Identify the blood parasite species.
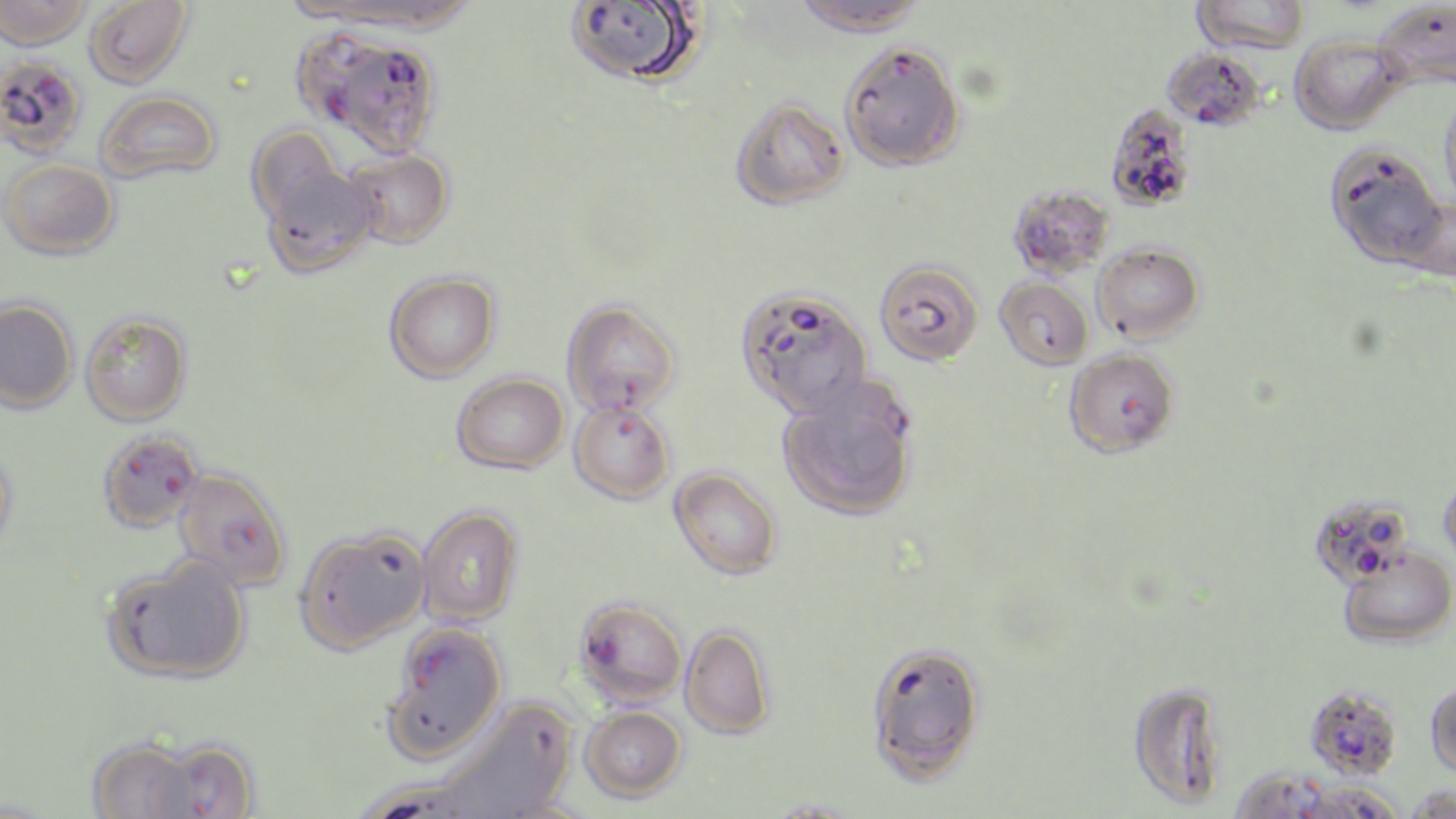

Plasmodium falciparum.

stain = May-Grünwald-Giemsa
magnification = 1000x
uninfected red blood cell locations = approximate bounding boxes as [x1, y1, x2, y2] in pixels: [0, 0, 91, 50], [84, 0, 192, 88], [325, 0, 478, 34], [565, 0, 704, 88], [792, 0, 928, 36], [1191, 0, 1310, 55], [1375, 0, 1456, 93], [293, 29, 377, 128], [1290, 34, 1403, 134], [839, 41, 965, 172], [1162, 48, 1266, 131], [96, 90, 221, 185], [1439, 96, 1456, 214], [730, 98, 849, 210], [1105, 104, 1198, 212], [246, 127, 344, 228], [1324, 143, 1448, 269], [346, 148, 454, 249], [1, 159, 118, 259], [260, 164, 378, 278], [1006, 183, 1115, 278], [1092, 243, 1205, 343], [875, 260, 983, 366], [384, 270, 501, 382], [995, 276, 1094, 370], [734, 284, 873, 419], [0, 298, 78, 413], [561, 299, 681, 416], [80, 311, 192, 426], [452, 372, 569, 473], [568, 398, 675, 504], [0, 447, 19, 560], [670, 467, 783, 580], [1438, 473, 1456, 570], [417, 505, 523, 627], [294, 525, 430, 654], [1338, 548, 1456, 647], [101, 553, 252, 685], [679, 624, 776, 739], [1126, 681, 1230, 809], [1425, 681, 1456, 780], [383, 687, 505, 767], [434, 698, 577, 819], [580, 705, 686, 802], [85, 735, 210, 819], [134, 736, 263, 818], [1230, 767, 1334, 819], [1294, 778, 1404, 819], [1406, 783, 1455, 819]
image size = 1456×819 pixels
field of view = single
modality = optical microscopy
Plasmodium falciparum-infected red blood cell locations = approximate bounding boxes as [x1, y1, x2, y2] in pixels: [333, 31, 435, 165], [0, 55, 88, 158], [1063, 348, 1180, 459], [789, 386, 916, 478], [96, 430, 204, 533], [173, 467, 292, 592], [1308, 492, 1416, 589], [573, 597, 688, 707], [403, 622, 509, 702], [865, 640, 987, 783], [1305, 684, 1403, 781]
preparation = thin blood film